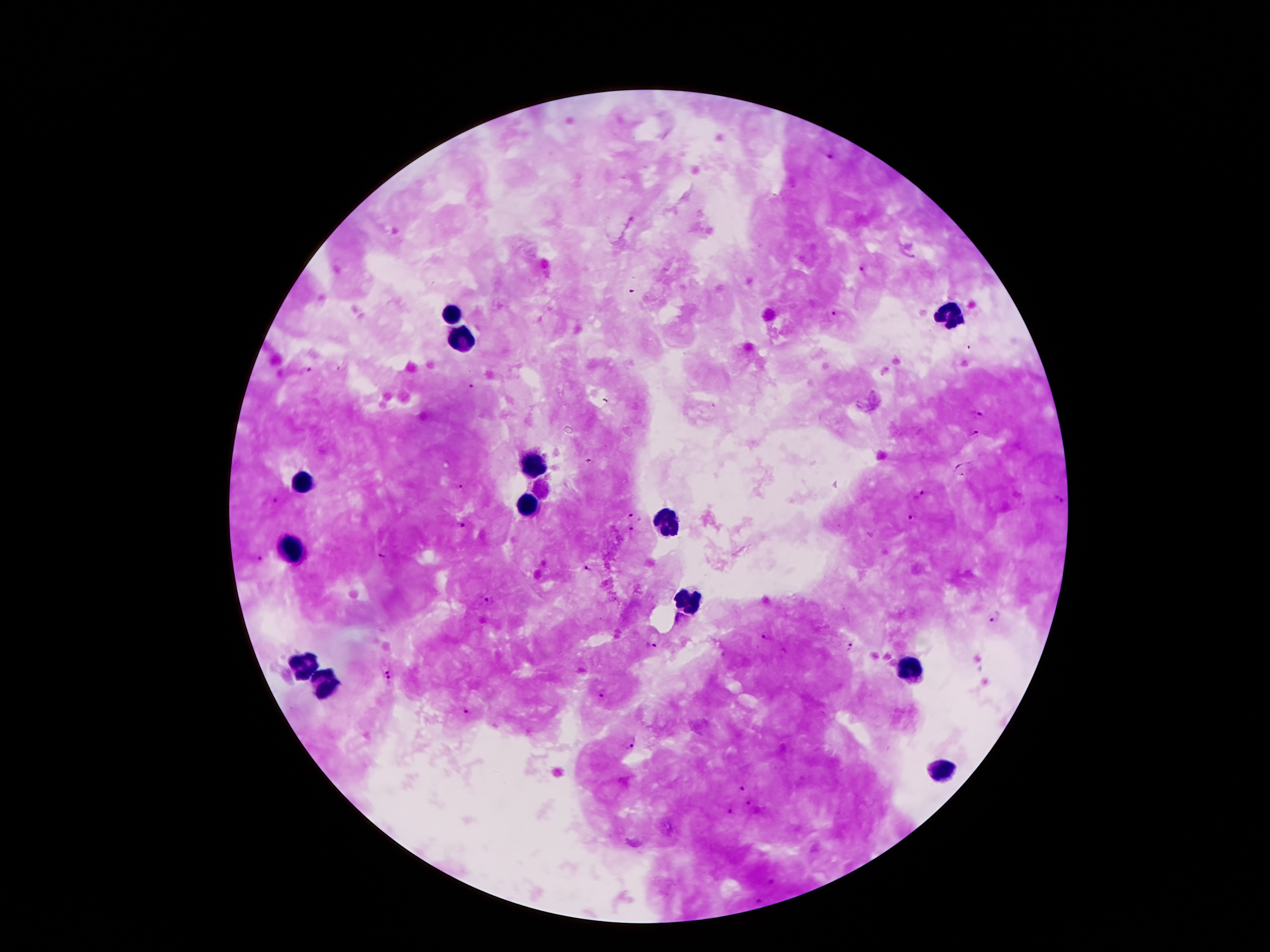
Approximate centers as {x, y} in pixels. Plasmodium parasite locations: {830, 157}, {861, 270}, {632, 292}, {834, 312}, {309, 369}, {470, 388}, {978, 415}, {974, 434}, {589, 462}, {460, 489}, {921, 493}, {1058, 498}, {276, 501}, {634, 515}, {909, 519}, {465, 528}, {631, 531}, {380, 556}, {258, 559}, {588, 568}, {490, 598}, {994, 617}, {765, 640}, {850, 645}, {650, 646}, {386, 675}, {602, 696}, {465, 710}, {628, 742}, {741, 789}, {750, 805}, {729, 813}, {770, 881}, {761, 902}. Leukocyte locations: {452, 313}, {948, 315}, {464, 339}, {532, 465}, {302, 483}, {528, 503}, {670, 523}, {290, 553}, {688, 603}, {302, 667}, {912, 673}, {324, 683}, {940, 769}. One field from this slide. Thick blood smear. Patient malaria status: positive for Plasmodium falciparum. Image is 1270×952 pixels. Giemsa stain. Smartphone photograph taken through the microscope eyepiece. 100x magnification.